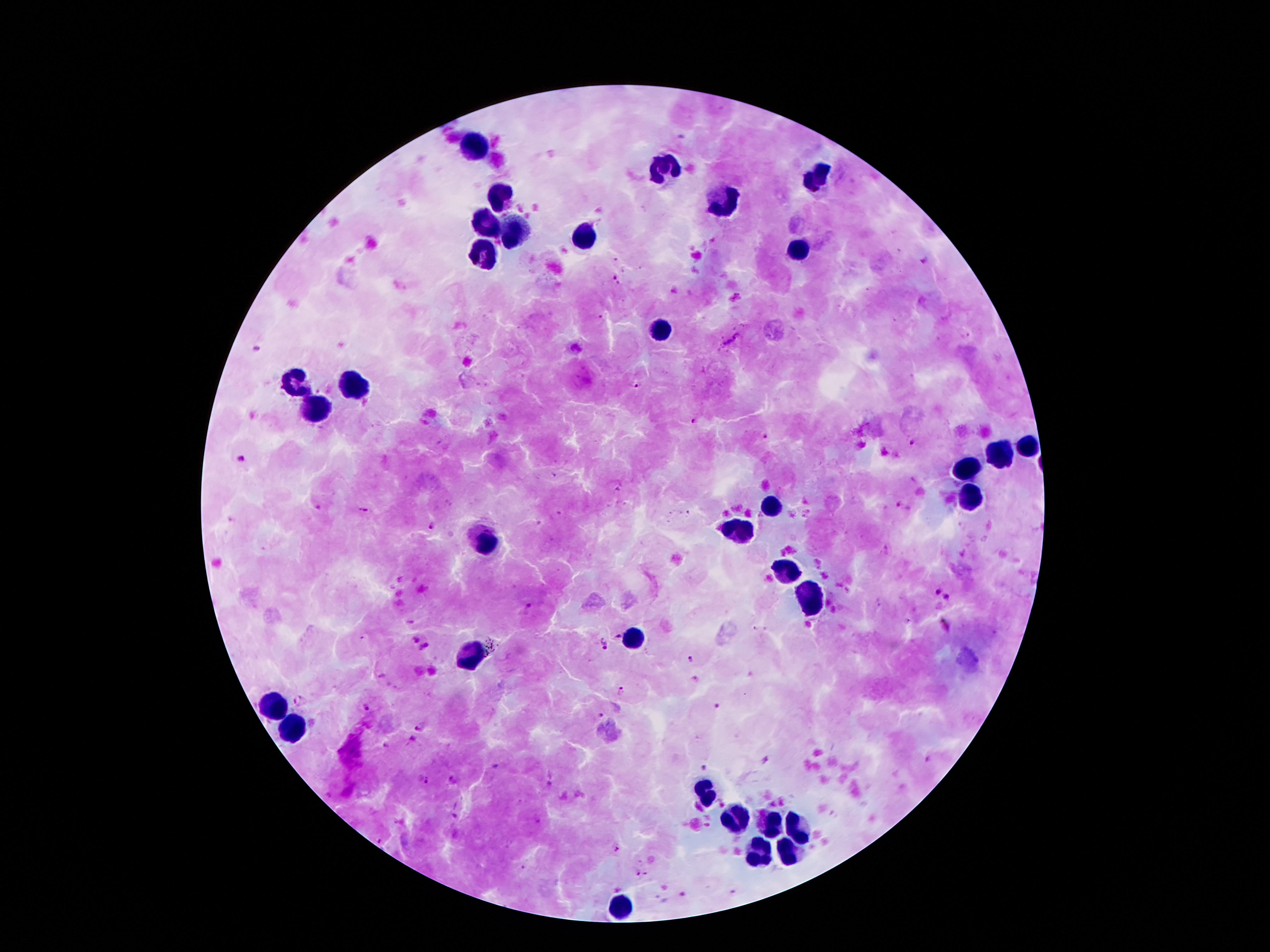 Approximate centers as (x, y) in pixels. Leukocyte locations: (474, 146), (661, 164), (817, 178), (502, 195), (726, 202), (488, 223), (516, 230), (586, 239), (798, 251), (484, 255), (663, 329), (355, 383), (297, 384), (320, 408), (1025, 449), (999, 455), (967, 468), (969, 496), (773, 504), (738, 528), (488, 543), (785, 570), (810, 600), (633, 638), (474, 652), (276, 704), (294, 727), (707, 792), (736, 822), (770, 825), (794, 825), (789, 850), (761, 854), (617, 905). Malaria parasite locations: (924, 260), (614, 277), (737, 335), (729, 342), (576, 347), (635, 385), (691, 422), (766, 434), (911, 442), (243, 458), (363, 510), (433, 527), (937, 592), (946, 596), (526, 606), (944, 625), (617, 635), (414, 639), (604, 644), (425, 646), (691, 660), (382, 677), (695, 680), (621, 689), (301, 700), (716, 706), (366, 708), (601, 715), (415, 728), (415, 741), (385, 745), (765, 759), (702, 767), (423, 780), (618, 850), (682, 895). Thick blood film. Giemsa-stained preparation. Patient malaria status: infected with Plasmodium falciparum. 100x magnification. One field from this slide. Photographed through the microscope eyepiece with a smartphone camera. Image is 1270×952 pixels.